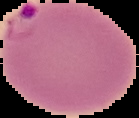
image_size: 139×118 pixels
image_type: segmented cell region on a black background
result: malaria parasites identified
preparation: thin blood film